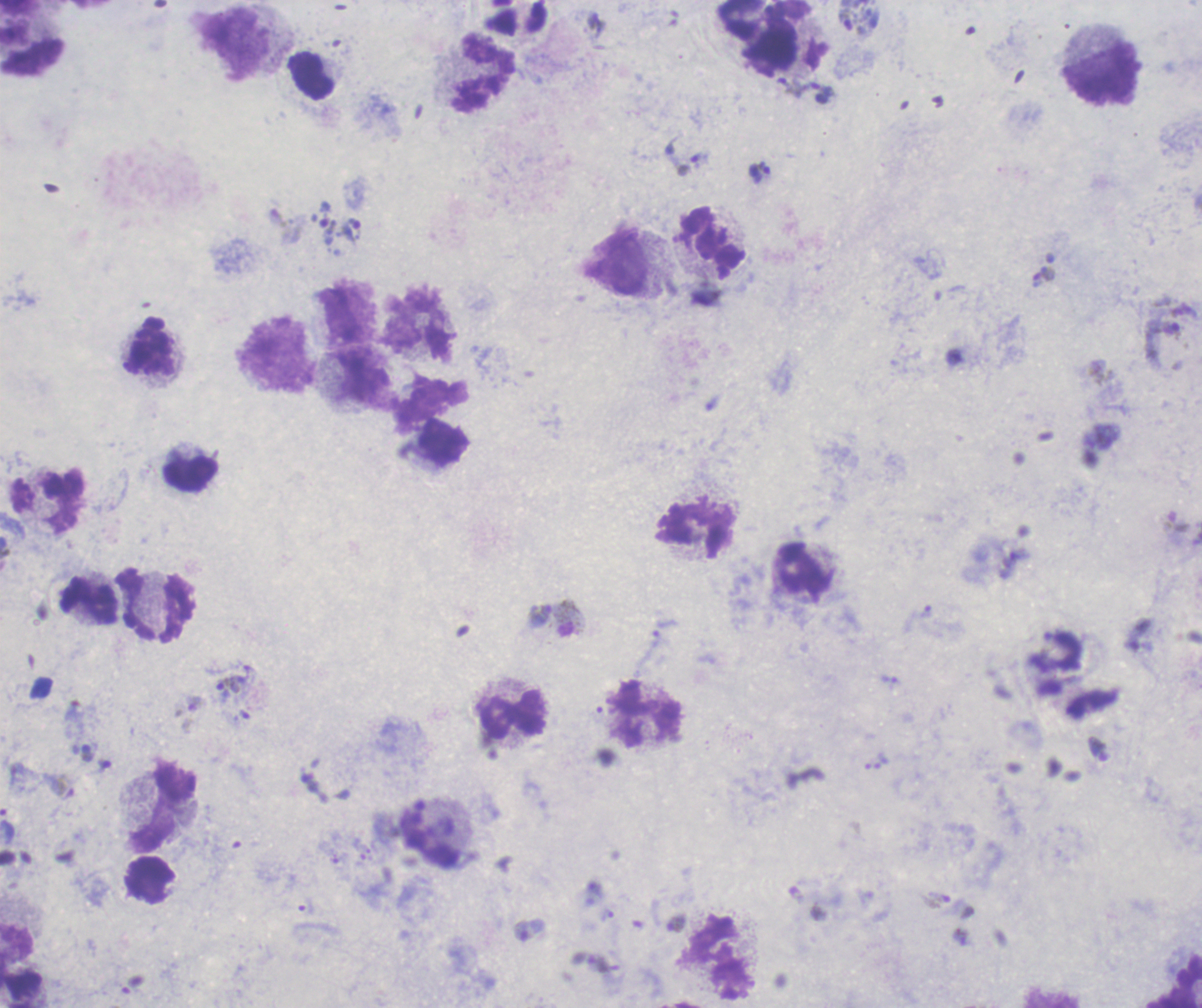

Approximate centers as (x, y) in pixels.
Summary:
  - Trophozoite locations: (851, 20), (792, 87), (822, 92), (687, 157), (759, 172), (323, 224), (352, 230), (1043, 276), (1166, 331), (926, 612), (569, 618), (232, 686), (197, 704), (937, 900), (607, 914), (676, 923), (529, 930)
  - Gametocyte locations: (84, 751)
  - Leukocyte locations: (763, 36), (31, 37), (234, 43), (484, 73), (1102, 75), (310, 76), (711, 241), (615, 262), (418, 328), (149, 347), (278, 355), (364, 378), (445, 443), (190, 474), (697, 528), (802, 571), (88, 600), (155, 605), (511, 714), (646, 714), (162, 806), (17, 947), (718, 958)
  - Life-cycle stages observed: trophozoite, gametocyte
  - Field of view: one from this slide
  - Stain: Romanowsky
  - Image size: 1202×1008 pixels
  - Context: previously used in a real diagnosis
  - Preparation: thick blood film
  - Background quality: poor
  - Result: positive for Plasmodium parasites
  - Magnification: 100x